Assess this cell for malaria.
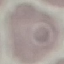

Uninfected.

Summary:
  - Preparation: thin blood smear
  - Image type: cell patch, automatically extracted from a larger field of view and resized to 64 × 64 pixels
  - Stain: Giemsa
  - Capture: smartphone camera at the microscope eyepiece